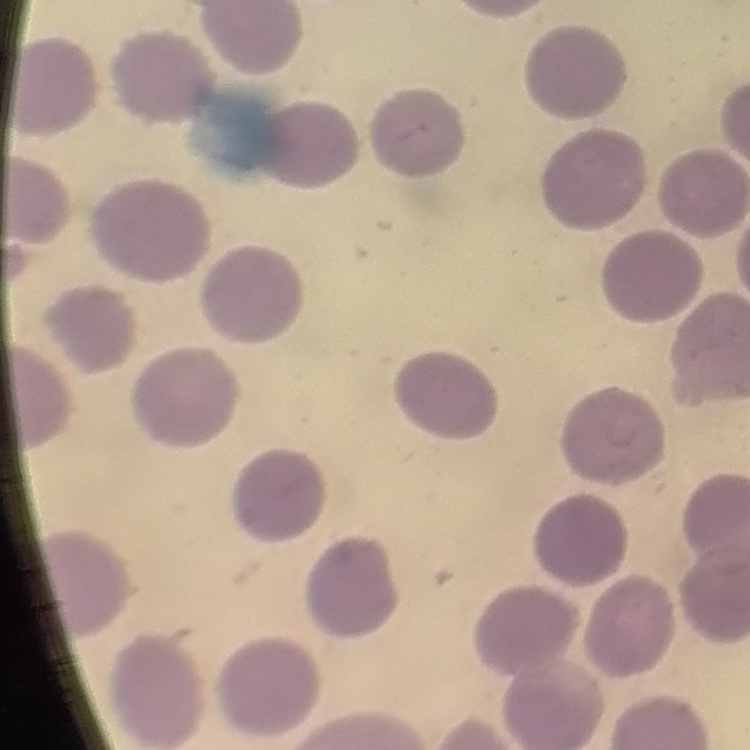

erythrocyte morphology = no rouleaux formation
stain = Field's or Giemsa
image type = one tile cut from a larger photomicrograph
preparation = thin peripheral smear